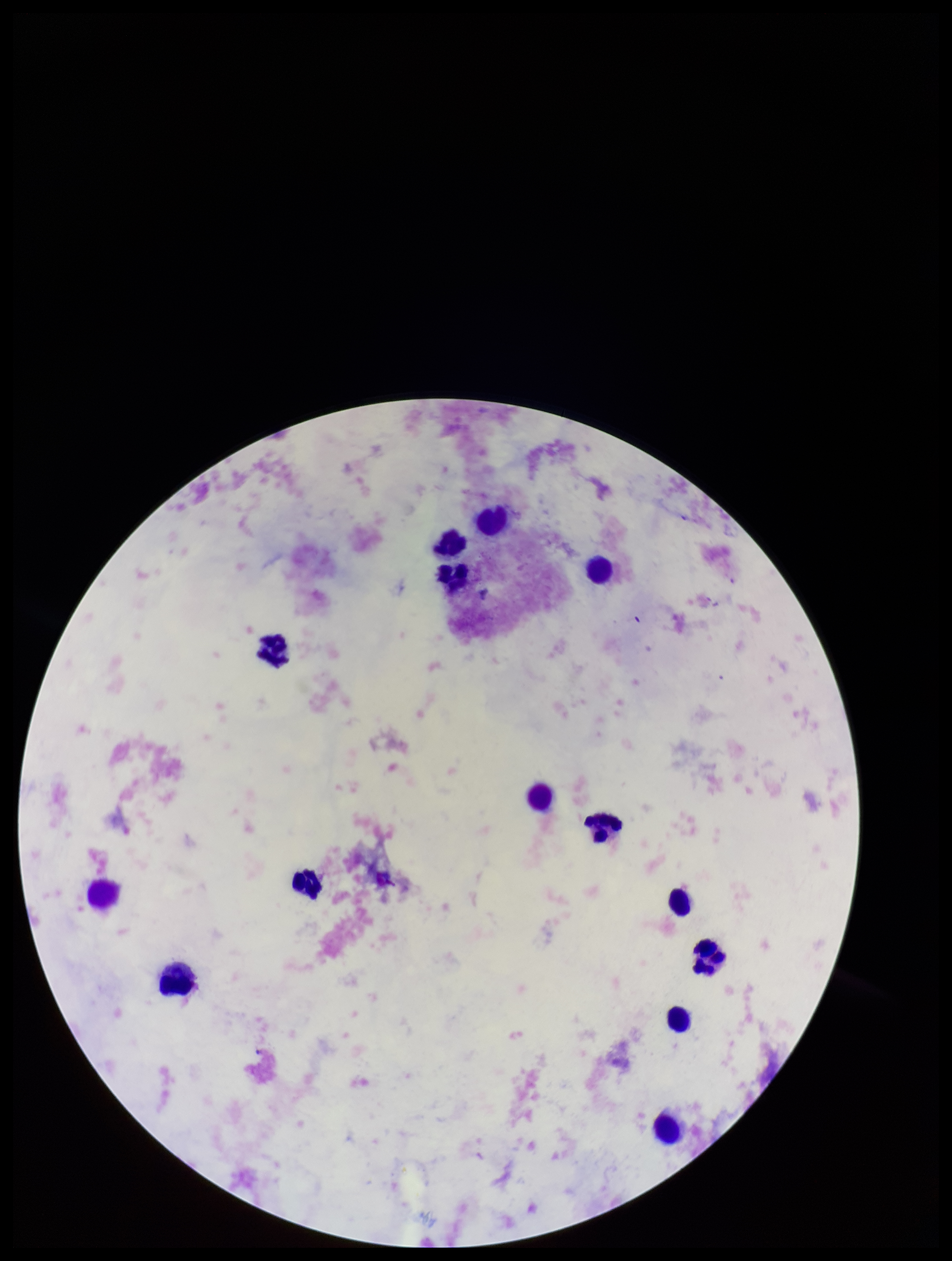
Summary:
  - Capture: smartphone photograph through the microscope eyepiece
  - Stain: Giemsa
  - Plasmodium parasites: none identified
  - Patient malaria status: negative
  - Field of view: one from this slide
  - Leukocyte count: 14
  - Parasite count: 0
  - Preparation: thick
  - Image size: 952×1261 pixels